Locate every Plasmodium falciparum-infected red blood cell.
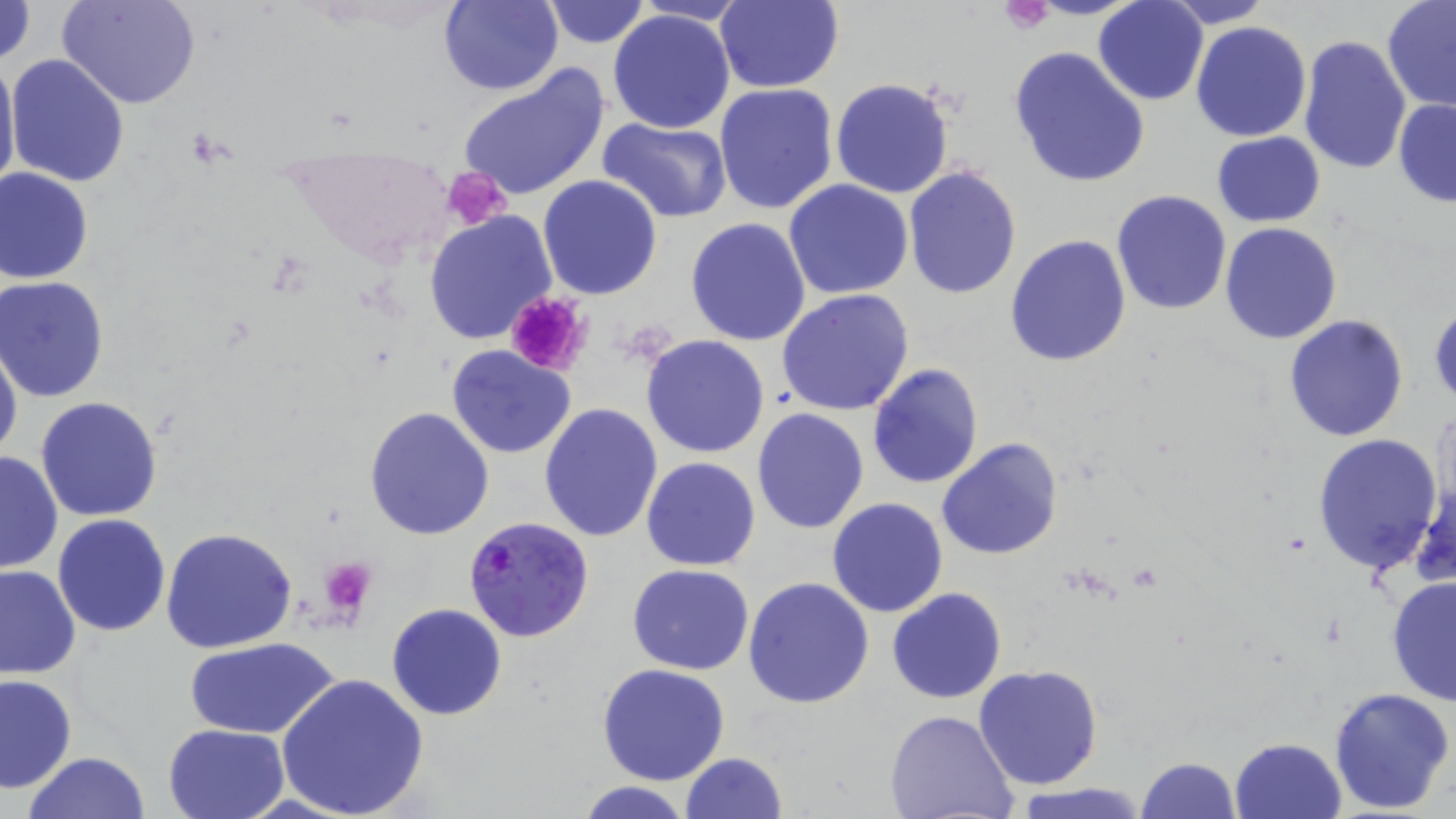
Approximate bounding boxes as (x1, y1, x2, y2) in pixels.
Plasmodium falciparum-infected red blood cells: (465, 517, 596, 642).

slide_level_diagnosis: Plasmodium falciparum
field_of_view: one of a larger specimen
preparation: thin blood film
platelet_locations: 'approximate bounding boxes as (x1, y1, x2, y2) in pixels: (999, 2, 1052, 32), (444, 166, 512, 229), (505, 289, 594, 378), (318, 556, 378, 613)'
uninfected_red_blood_cell_locations: 'approximate bounding boxes as (x1, y1, x2, y2) in pixels: (0, 0, 36, 67), (59, 0, 201, 109), (438, 0, 565, 96), (541, 0, 649, 47), (714, 0, 842, 93), (1159, 0, 1275, 26), (634, 1, 753, 25), (1093, 1, 1209, 105), (1382, 2, 1456, 112), (608, 9, 736, 133), (1189, 20, 1312, 142), (1298, 35, 1413, 177), (1009, 46, 1151, 188), (0, 49, 20, 202), (5, 54, 130, 188), (456, 64, 610, 203), (830, 76, 955, 199), (713, 82, 839, 213), (1392, 99, 1456, 208), (599, 118, 732, 221), (1210, 132, 1326, 227), (901, 166, 1021, 299), (1, 168, 95, 284), (537, 175, 664, 300), (784, 178, 914, 300), (1111, 190, 1232, 315), (424, 209, 557, 345), (685, 217, 812, 347), (1220, 222, 1342, 344), (1005, 234, 1132, 367), (0, 276, 108, 401), (776, 288, 916, 414), (1428, 299, 1455, 409), (1282, 314, 1410, 443), (641, 335, 771, 458), (0, 336, 22, 469), (446, 344, 577, 459), (867, 362, 984, 489), (36, 397, 164, 521), (539, 402, 665, 543), (1431, 406, 1455, 528), (364, 407, 496, 540), (752, 408, 869, 534), (1312, 433, 1444, 574), (938, 437, 1062, 560), (0, 449, 62, 575), (641, 457, 761, 571), (1411, 468, 1455, 593), (826, 497, 949, 619), (53, 513, 171, 636), (160, 527, 297, 652), (0, 563, 79, 680), (626, 564, 754, 675), (1387, 572, 1456, 709), (743, 576, 874, 707), (886, 587, 1007, 704), (387, 603, 507, 720), (187, 636, 339, 740), (597, 663, 731, 786), (975, 664, 1104, 791), (275, 670, 428, 819), (0, 674, 76, 794), (1328, 686, 1454, 813), (886, 711, 1020, 819), (163, 722, 291, 818), (1230, 737, 1347, 819), (24, 751, 149, 819), (681, 752, 787, 819), (1135, 757, 1239, 818), (572, 780, 697, 819), (1013, 784, 1151, 819)'
modality: light microscopy
magnification: 1000x
stain: May-Grünwald-Giemsa
image_size: 1456×819 pixels